Identify the parasite.
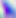

This is Toxoplasma gondii.

Summary:
  - Modality: micrograph
  - Magnification: 400x